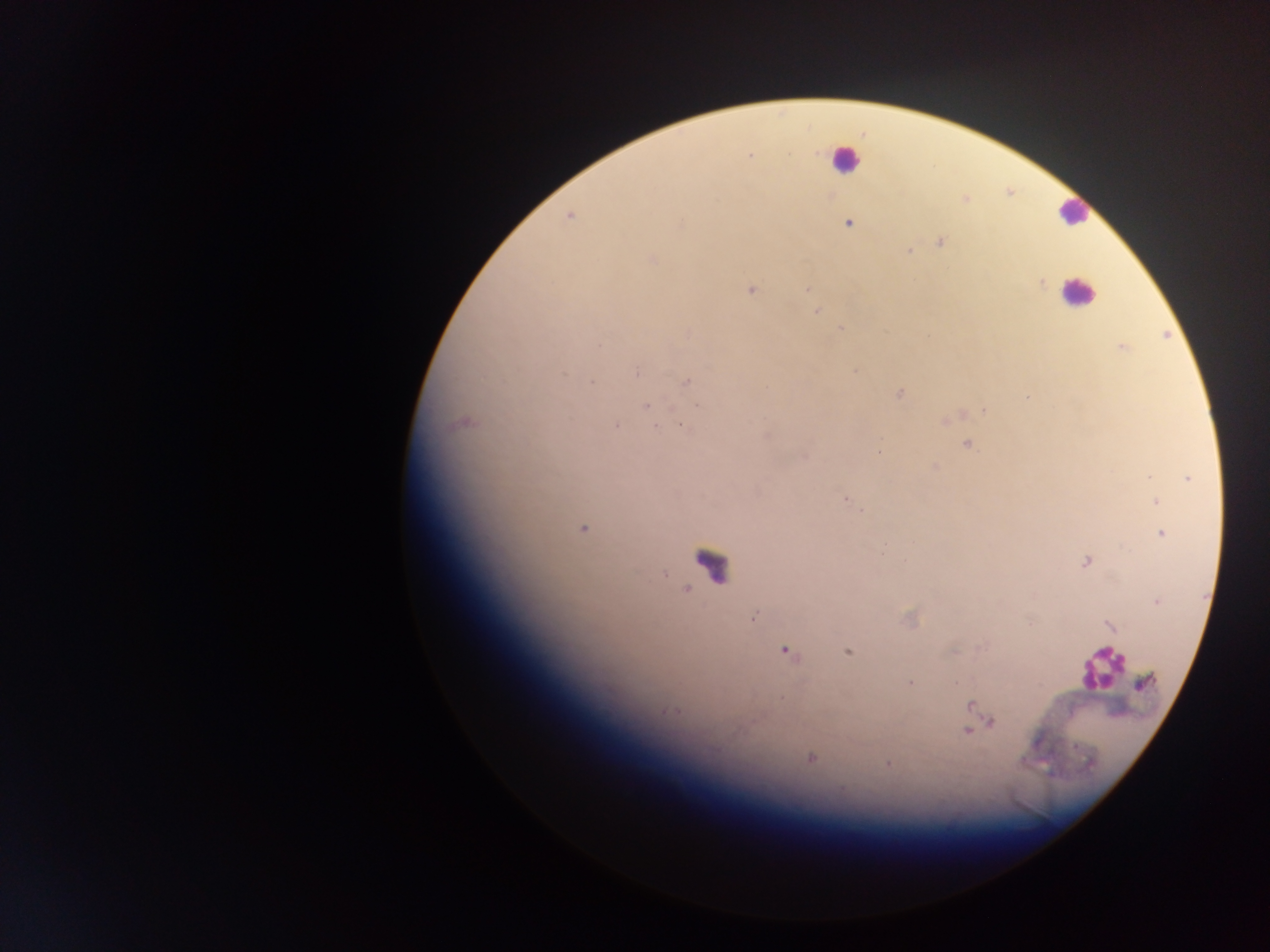
Approximate centers as x y in pixels. Plasmodium parasite locations: 750 157; 965 199; 569 216; 848 224; 940 242; 909 251; 653 260; 1042 283; 808 289; 751 290; 816 311; 842 327; 599 345; 1122 348; 855 371; 637 374; 591 381; 688 381; 900 393; 1027 397; 646 405; 698 405; 983 410; 616 426; 655 427; 682 427; 766 436; 966 444; 879 452; 935 467; 1149 476; 1188 478; 845 499; 1155 502; 861 511; 583 529; 1162 533; 1085 562; 1156 602; 753 617; 1029 623; 1110 626; 785 651; 847 651; 955 652; 956 682; 910 683; 1144 683; 781 697; 970 705; 665 711; 992 721; 966 732; 811 758; 887 763. Leukocyte locations: 844 159; 1074 213; 1077 292; 711 563; 1100 668. Sample from Ghana. Thick blood smear. Mobile-phone photograph taken through the microscope. Image is 1270×952 pixels. Single field of view.